Comment on the morphology of the erythrocytes.
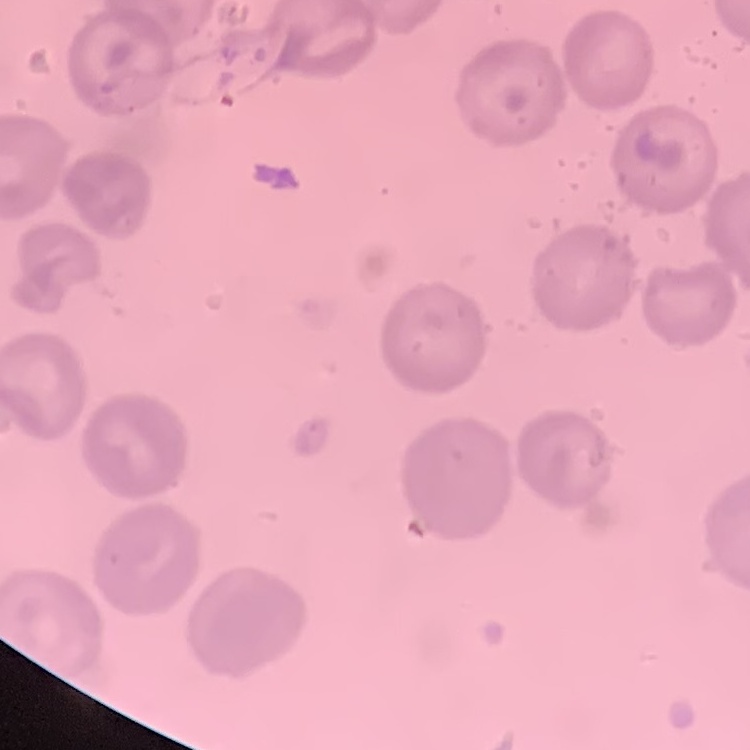

No rouleaux formation.

Summary:
  - Preparation: thin blood smear
  - Stain: Field's or Giemsa
  - Image type: square crop of a larger photomicrograph